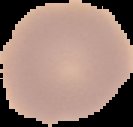

Image is 133×127 pixels. The area outside the segmented cell region is set to black. From a thin blood film. Malaria status: uninfected.